Locate every malaria parasite.
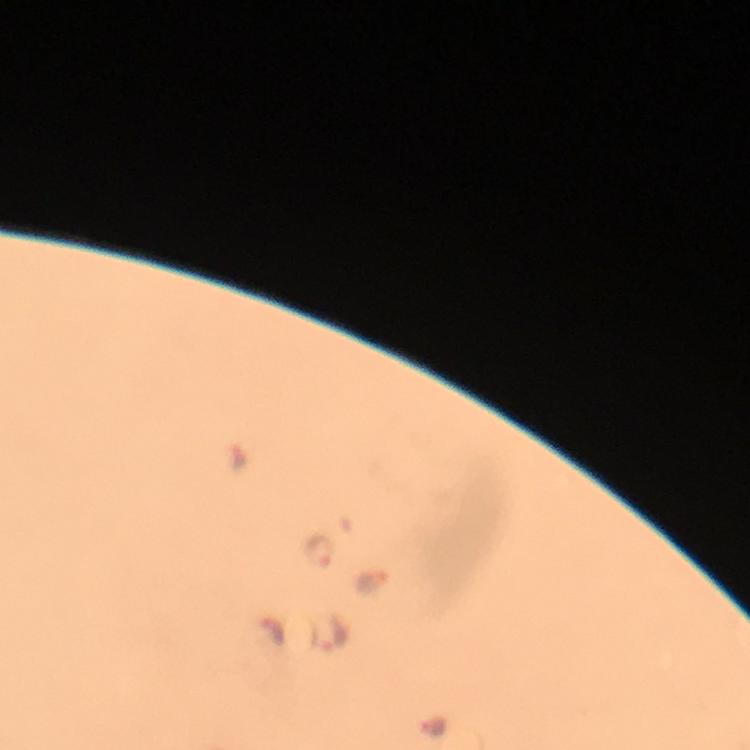

Approximate centers as (x, y) in pixels.
Malaria parasites: (318, 551), (374, 581), (273, 631), (337, 634), (432, 726).

From a malaria diagnostic workup. 100x magnification. Cropped region of a single field of view. Photographed with a smartphone mounted on the microscope. Immersion oil applied. Thick blood film. Giemsa-stained preparation. Image is 750×750 pixels.